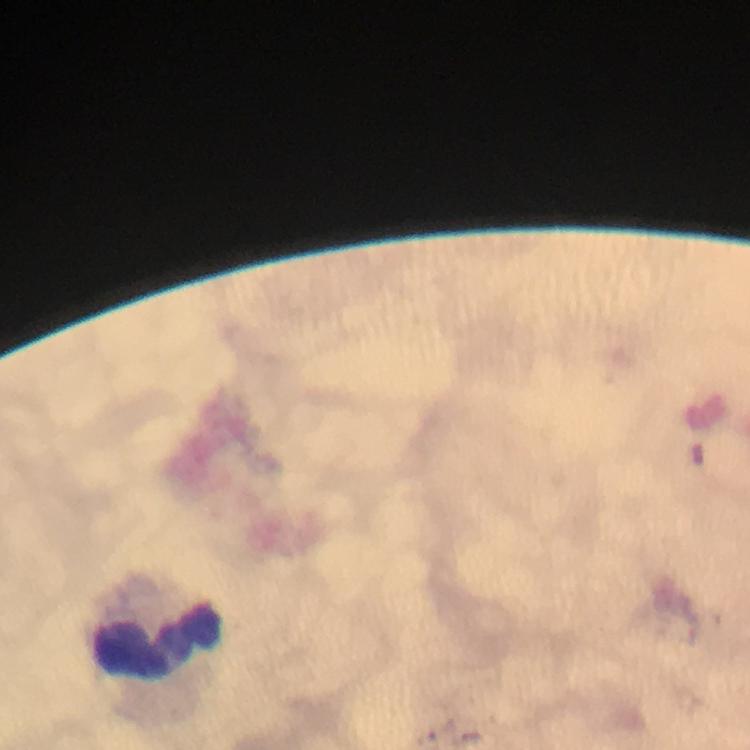

Approximate object centers, in pixels from the top-left corner. Leukocyte locations: (x=160, y=643). A crop from one field of view. Plasmodium parasites: none detected. Photographed through the microscope with a smartphone camera. Image is 750×750 pixels. Giemsa stain. At 100x magnification. From a diagnostic examination for malaria. Thick blood smear. Immersion oil applied.